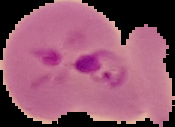

image size = 175×127 pixels
result = Plasmodium parasites detected
preparation = thin blood smear
image type = segmented cell region on a black background